Outline each uninfected red blood cell.
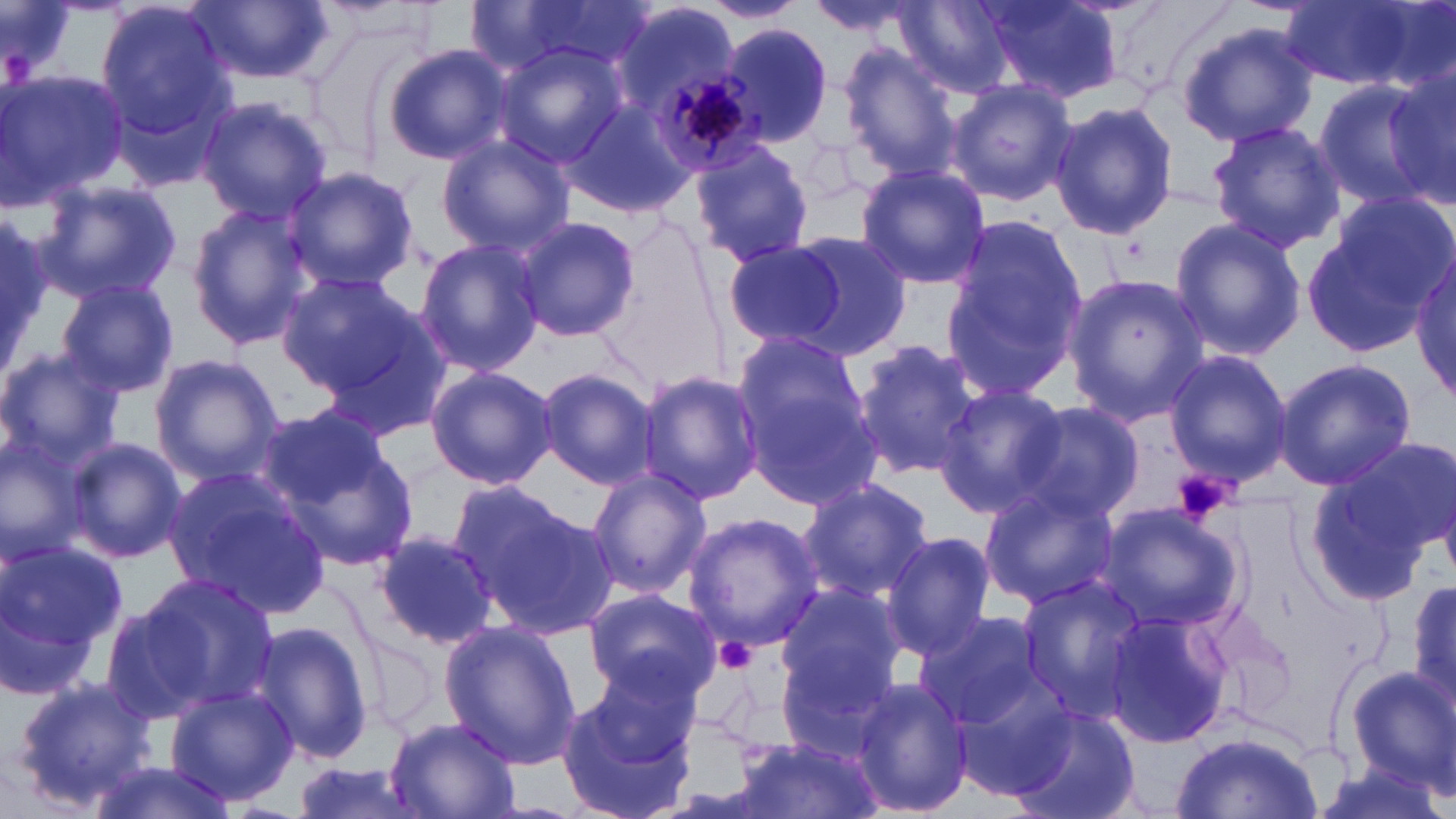
Approximate bounding boxes as (x1, y1, x2, y2) in pixels.
Uninfected red blood cells: (194, 0, 336, 85), (472, 0, 652, 79), (895, 0, 1013, 98), (696, 1, 806, 24), (977, 1, 1121, 103), (1282, 1, 1438, 91), (95, 2, 235, 143), (611, 2, 744, 133), (801, 2, 927, 37), (1175, 21, 1318, 147), (720, 23, 833, 144), (492, 42, 629, 174), (383, 44, 515, 165), (841, 48, 960, 175), (1384, 63, 1456, 211), (0, 68, 129, 210), (944, 78, 1076, 207), (1311, 78, 1443, 207), (194, 96, 333, 224), (559, 96, 694, 216), (1048, 100, 1178, 243), (1206, 120, 1345, 252), (436, 135, 574, 258), (689, 140, 815, 268), (853, 164, 991, 287), (283, 166, 417, 293), (35, 179, 183, 304), (186, 202, 312, 350), (1299, 202, 1445, 357), (0, 211, 52, 360), (941, 212, 1092, 403), (513, 214, 642, 343), (1168, 216, 1307, 361), (787, 232, 914, 358), (414, 237, 545, 376), (721, 239, 848, 349), (1412, 258, 1455, 407), (274, 270, 421, 395), (1061, 273, 1208, 425), (55, 277, 180, 398), (302, 297, 453, 438), (850, 338, 985, 482), (731, 343, 881, 510), (0, 347, 125, 473), (1165, 351, 1291, 484), (149, 352, 284, 484), (1273, 357, 1417, 492), (425, 365, 557, 490), (537, 367, 659, 490), (636, 371, 766, 505), (934, 385, 1067, 518), (1009, 397, 1150, 524), (256, 405, 418, 574), (0, 429, 91, 562), (65, 438, 186, 565), (1309, 442, 1450, 599), (161, 466, 332, 622), (584, 468, 711, 599), (797, 476, 935, 603), (443, 477, 573, 600), (976, 480, 1120, 607), (465, 494, 618, 641), (1099, 501, 1243, 630), (683, 511, 824, 650), (368, 531, 500, 650), (881, 532, 995, 659), (0, 533, 126, 690), (126, 572, 280, 716), (1408, 572, 1456, 718), (1015, 574, 1148, 716), (774, 583, 906, 703), (586, 589, 723, 701), (100, 601, 214, 723), (1102, 608, 1236, 750), (912, 611, 1050, 733), (250, 617, 378, 767), (439, 621, 584, 769), (356, 626, 442, 740), (774, 653, 898, 763), (588, 655, 706, 767), (1341, 665, 1456, 792), (9, 674, 160, 811), (849, 676, 973, 819), (165, 685, 297, 806), (557, 688, 692, 819), (1011, 707, 1141, 819), (383, 717, 520, 818), (1173, 730, 1321, 819), (732, 738, 883, 819), (85, 758, 238, 819), (288, 760, 421, 819).

Summary:
  - Platelet locations: (1171, 469, 1238, 521), (718, 637, 758, 671)
  - Plasmodium malariae-infected red blood cell locations: (656, 63, 769, 178)
  - Slide-level diagnosis: Plasmodium malariae
  - Field of view: single
  - Stain: May-Grünwald-Giemsa
  - Preparation: thin blood smear
  - Magnification: 1000x
  - Image size: 1456×819 pixels
  - Modality: light microscopy